Assess this cell for malaria.
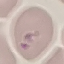

It is parasitized.

Acquired by smartphone through the microscope eyepiece. Thin blood smear. Cell patch, automatically extracted from a larger field of view and resized to 64 × 64 pixels. Giemsa-stained preparation.